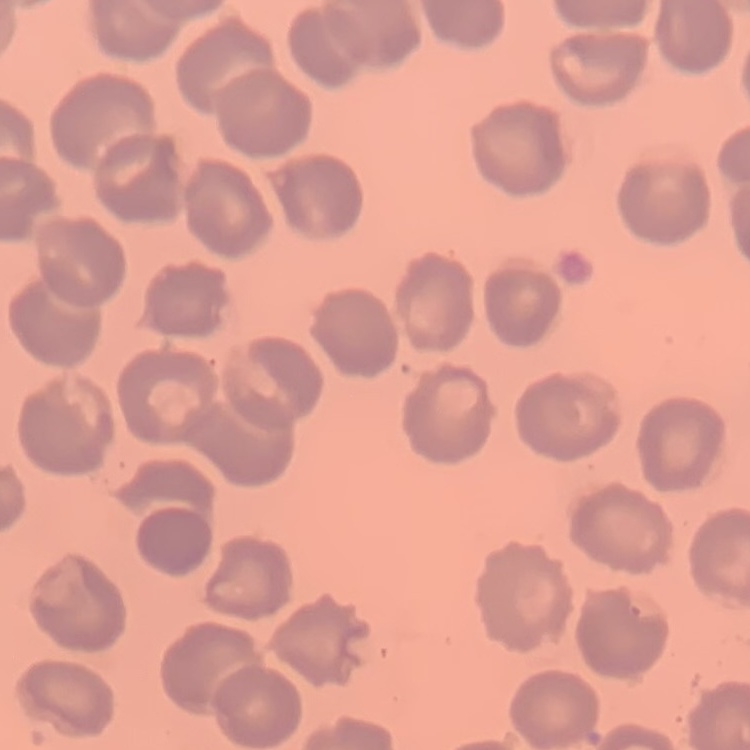

erythrocyte_morphology: no rouleaux formation
preparation: thin peripheral smear
stain: Field's or Giemsa
image_type: square crop of a larger photomicrograph